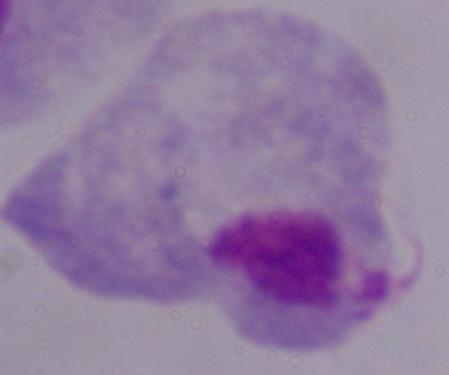

Photomicrograph. 1000x magnification. A trichomonad is seen.